Locate every Plasmodium parasite.
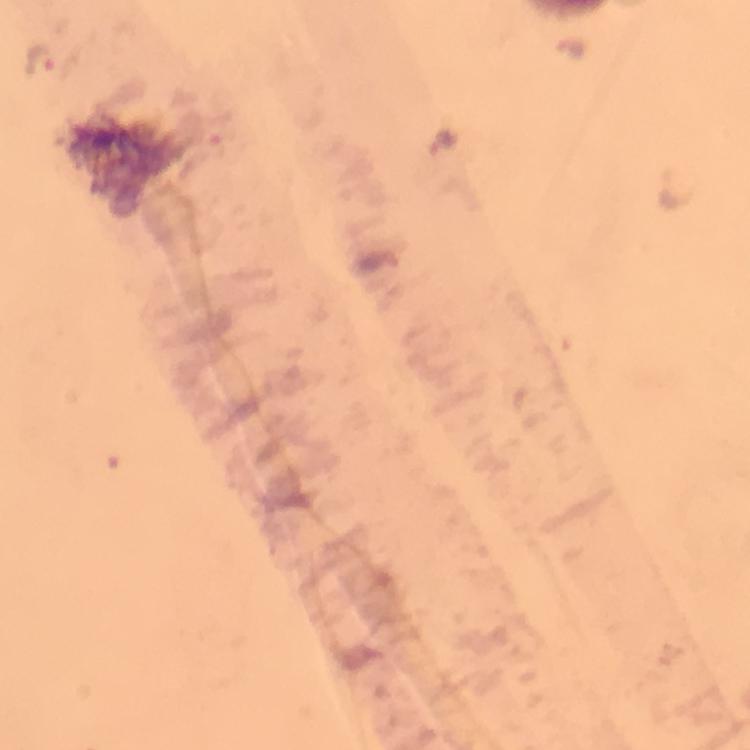

Approximate centers as (x, y) in pixels.
Plasmodium parasites: (570, 47), (41, 58), (444, 140), (672, 189).

A crop from one field of view. Immersion oil applied. Thick smear. 100x magnification. From a diagnostic examination for malaria. Giemsa-stained preparation. Photographed through the microscope with a smartphone camera. Image is 750×750 pixels.